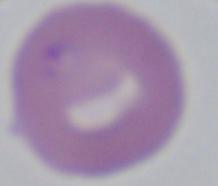
Summary:
  - Modality: photomicrograph
  - Identification: Babesia
  - Magnification: 1000x